Locate every Plasmodium parasite.
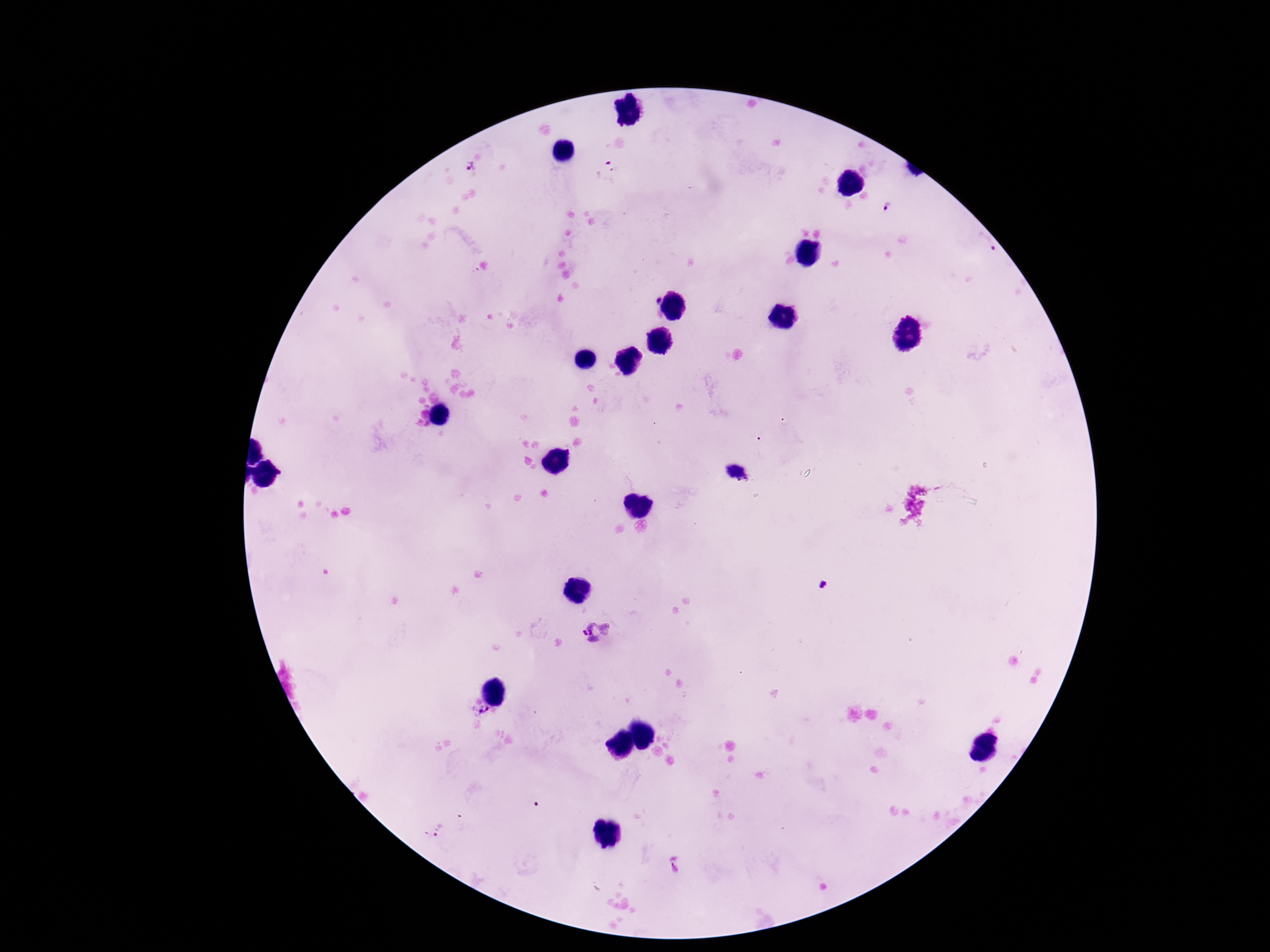
Approximate centers as [x, y] in pixels.
Plasmodium parasites: [469, 166], [608, 172], [887, 206], [985, 242], [657, 300], [598, 632], [481, 713], [439, 829], [675, 864].

magnification: 100x
preparation: thick peripheral-blood smear
field_of_view: single
patient_malaria_status: positive
stain: Giemsa
capture: smartphone camera through the microscope eyepiece
image_size: 1270×952 pixels